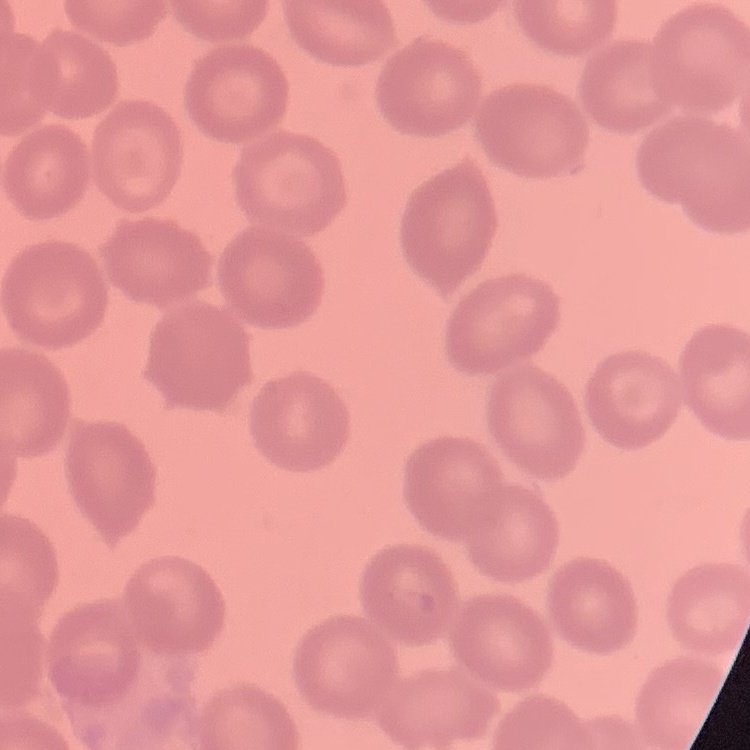
{
  "red_blood_cell_morphology": "no rouleaux formation",
  "preparation": "thin peripheral smear",
  "image_type": "square crop of a larger photomicrograph",
  "stain": "Field's or Giemsa"
}